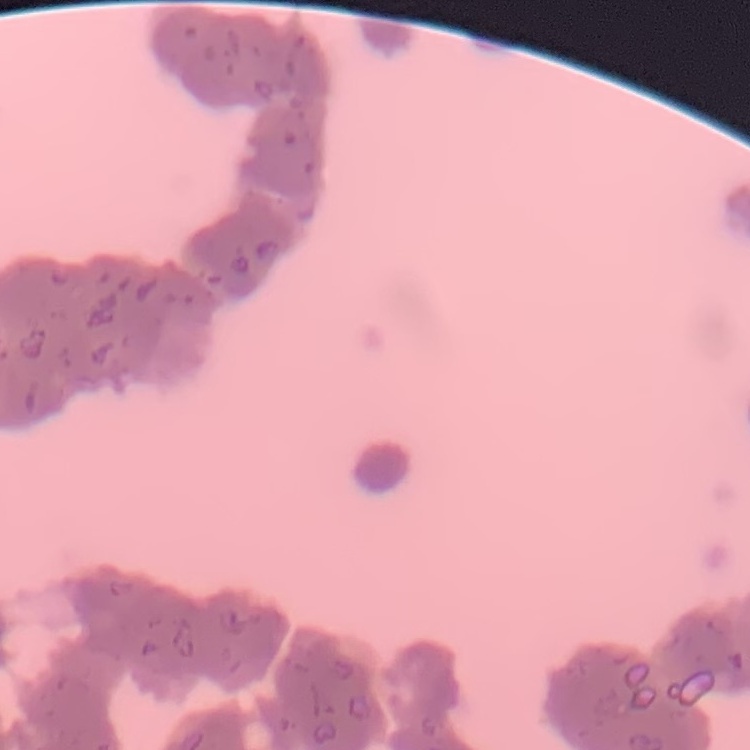

The erythrocytes exhibit rouleaux formation. Thin blood film. One tile cut from a larger photomicrograph. Stained with either Field's or Giemsa.